Name the blood parasite species.
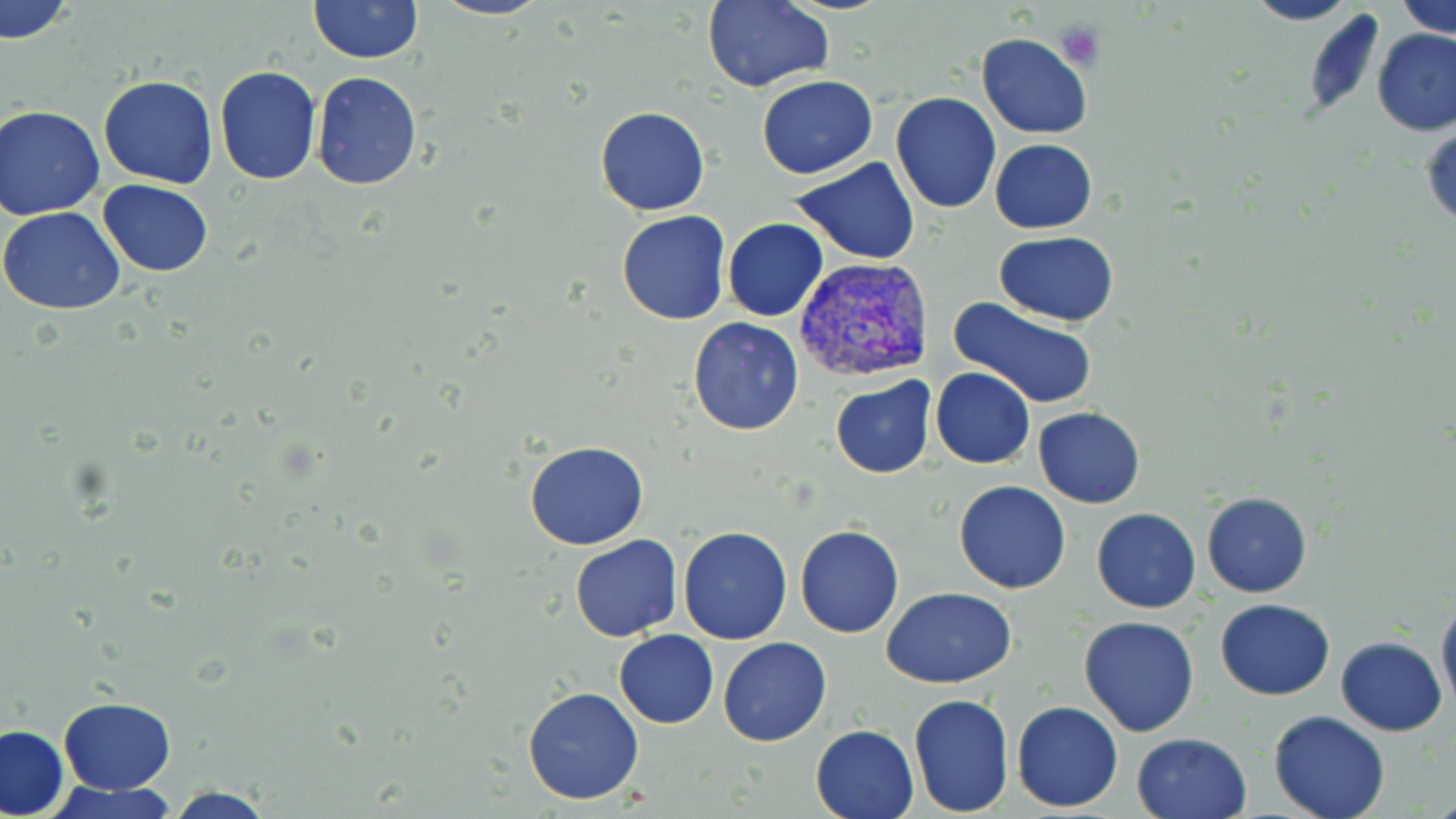
Plasmodium vivax.

Summary:
  - Coordinate format: approximate bounding boxes as (x1, y1, x2, y2) in pixels
  - Plasmodium vivax-infected red blood cell locations: (792, 257, 933, 384)
  - Uninfected red blood cell locations: (1, 0, 75, 44), (310, 0, 421, 63), (431, 0, 553, 20), (1395, 0, 1455, 37), (702, 1, 833, 91), (1243, 1, 1360, 26), (1300, 13, 1387, 113), (1372, 28, 1456, 137), (976, 32, 1092, 139), (214, 66, 321, 183), (312, 72, 422, 191), (757, 75, 877, 179), (97, 76, 218, 187), (891, 91, 1002, 214), (1, 105, 106, 219), (594, 106, 709, 215), (1422, 123, 1455, 230), (990, 139, 1097, 234), (793, 158, 921, 266), (97, 179, 213, 276), (0, 207, 127, 313), (617, 210, 731, 325), (724, 218, 827, 321), (993, 232, 1122, 325), (947, 297, 1099, 411), (689, 317, 804, 436), (930, 367, 1035, 469), (829, 377, 937, 479), (1033, 407, 1145, 508), (524, 441, 650, 550), (953, 481, 1072, 594), (1202, 492, 1312, 597), (1091, 508, 1201, 614), (796, 526, 904, 639), (678, 527, 793, 645), (570, 535, 683, 641), (882, 587, 1017, 688), (1437, 592, 1456, 715), (1215, 599, 1335, 700), (1078, 616, 1201, 737), (614, 630, 719, 728), (718, 636, 831, 746), (1337, 637, 1446, 736), (521, 685, 645, 805), (908, 693, 1015, 817), (58, 696, 177, 795), (1011, 701, 1124, 812), (1268, 711, 1392, 819), (810, 724, 919, 819), (1, 725, 69, 818), (1132, 732, 1253, 819), (47, 778, 178, 818), (161, 786, 278, 818)
  - Platelet locations: (1052, 18, 1106, 72)
  - Magnification: 1000x
  - Stain: May-Grünwald-Giemsa
  - Field of view: single
  - Preparation: thin blood smear
  - Image size: 1456×819 pixels
  - Modality: optical microscopy